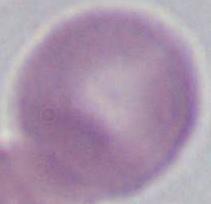

Summary:
  - Identification: erythrocyte
  - Magnification: 1000x
  - Modality: micrograph